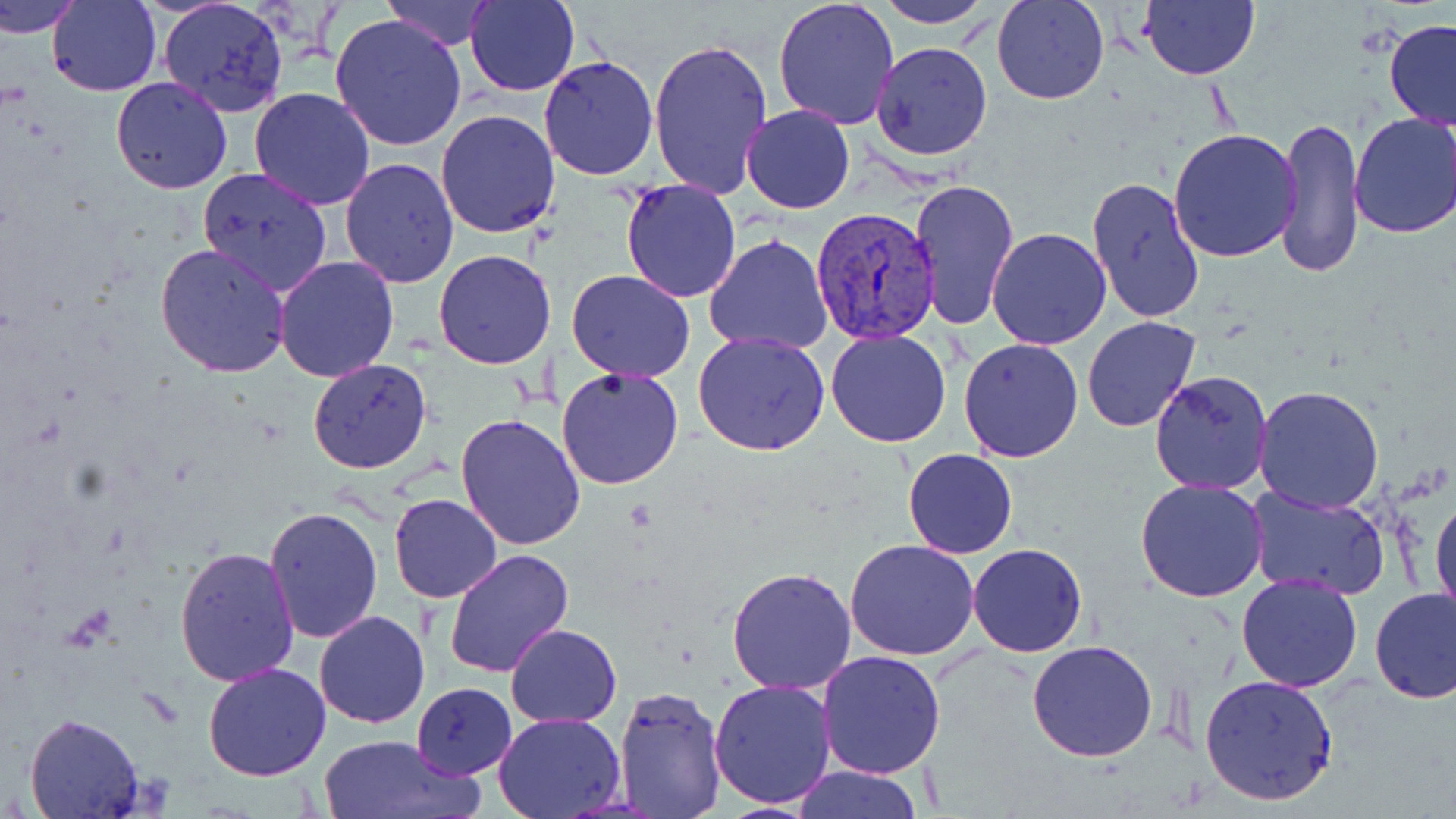
slide_level_diagnosis: Plasmodium vivax
stain: May-Grünwald-Giemsa
preparation: thin blood film
plasmodium_vivax_infected_red_blood_cell_locations: 'approximate bounding boxes as (x1, y1, x2, y2) in pixels: (811, 204, 943, 345)'
magnification: 1000x
field_of_view: single
image_size: 1456×819 pixels
uninfected_red_blood_cell_locations: 'approximate bounding boxes as (x1, y1, x2, y2) in pixels: (0, 0, 86, 37), (46, 0, 161, 97), (383, 0, 494, 50), (464, 0, 580, 97), (773, 0, 900, 130), (876, 0, 990, 29), (991, 0, 1109, 105), (1139, 0, 1259, 81), (159, 1, 290, 117), (329, 14, 466, 152), (1384, 18, 1456, 132), (648, 36, 774, 201), (870, 41, 993, 161), (537, 56, 659, 181), (111, 76, 233, 194), (249, 86, 378, 211), (741, 105, 855, 214), (435, 109, 560, 238), (1349, 112, 1456, 238), (1277, 116, 1365, 279), (1167, 129, 1301, 263), (339, 157, 459, 288), (196, 167, 334, 298), (1086, 175, 1205, 324), (909, 177, 1021, 333), (621, 180, 743, 302), (987, 227, 1111, 349), (704, 235, 835, 355), (156, 242, 291, 377), (433, 249, 557, 369), (274, 256, 400, 382), (568, 269, 695, 384), (1081, 316, 1200, 433), (826, 329, 952, 448), (692, 331, 831, 457), (958, 337, 1086, 463), (307, 358, 432, 474), (557, 367, 684, 489), (1150, 371, 1274, 494), (1254, 386, 1385, 514), (455, 412, 586, 551), (903, 449, 1019, 559), (1135, 478, 1270, 603), (1246, 485, 1389, 599), (1432, 490, 1456, 625), (389, 492, 503, 603), (408, 502, 539, 648), (262, 506, 383, 645), (846, 540, 980, 660), (968, 542, 1088, 657), (174, 546, 301, 688), (443, 547, 575, 678), (726, 567, 857, 694), (1236, 574, 1364, 693), (1369, 586, 1456, 703), (314, 611, 431, 729), (504, 624, 621, 728), (1027, 639, 1157, 763), (817, 649, 946, 777), (203, 663, 332, 781), (1198, 674, 1339, 807), (709, 679, 838, 810), (410, 682, 518, 778), (613, 685, 728, 818), (23, 712, 145, 817), (494, 713, 623, 819), (319, 733, 480, 819), (791, 764, 924, 819)'
modality: light microscopy